Assess this cell for malaria.
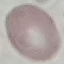
Uninfected.

preparation = thin smear
stain = Giemsa
image type = cell patch, automatically extracted from a larger field of view and resized to 64 × 64 pixels
capture = smartphone through the microscope eyepiece